Assess this cell for malaria.
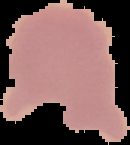
Uninfected.

Summary:
  - Preparation: thin blood smear
  - Image type: segmented cell region with the area outside set to black
  - Image size: 130×145 pixels